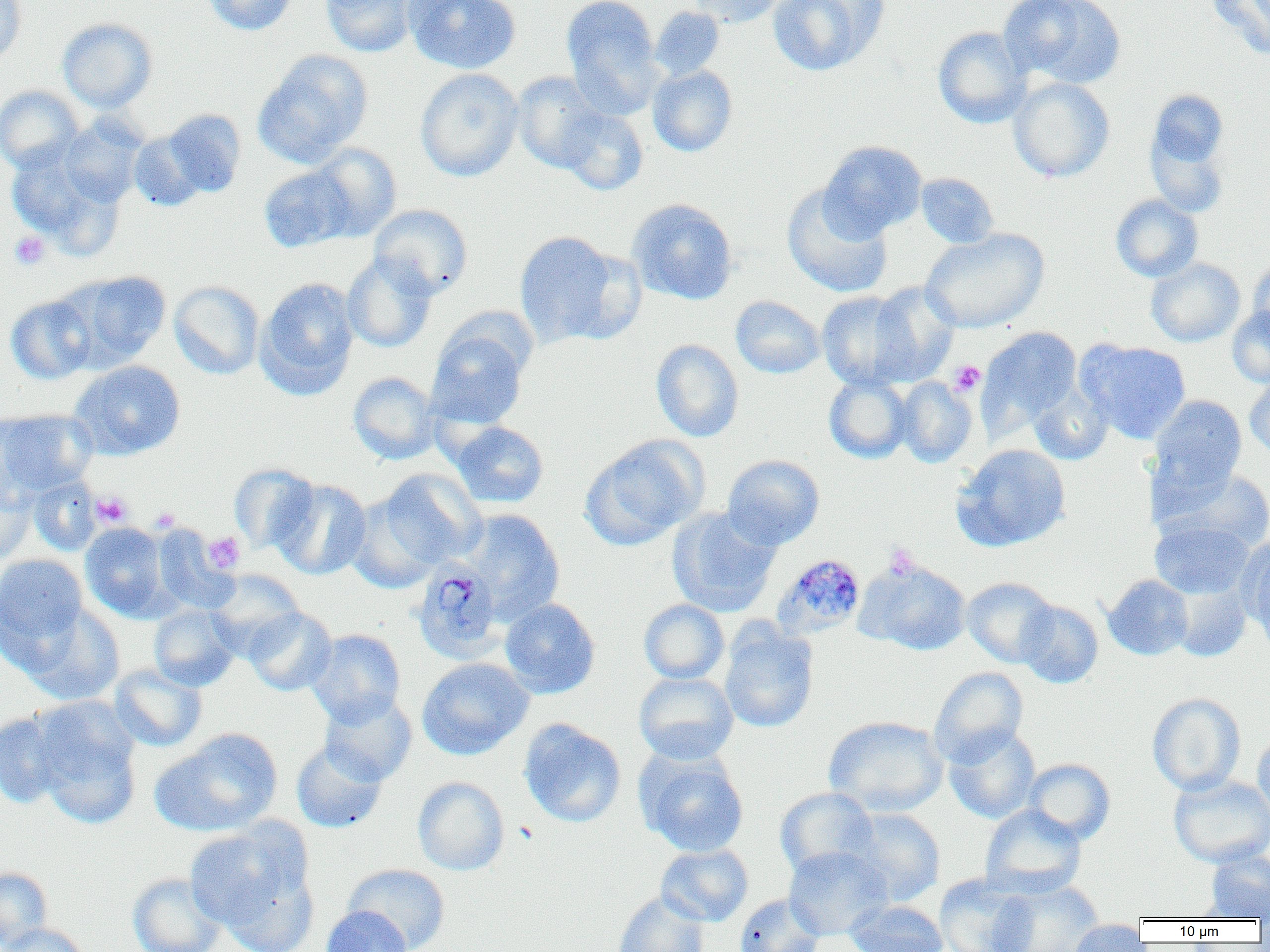 Approximate bounding boxes as (x1,y1)-(x2,y2) corner pairs in pixels. Uninfected red blood cell locations: (0,0)-(27,66), (202,0)-(298,36), (320,0)-(417,57), (404,0)-(521,74), (561,0)-(663,110), (689,0)-(789,27), (767,0)-(887,76), (998,0)-(1126,89), (1207,0)-(1270,58), (650,6)-(725,80), (57,18)-(158,112), (932,26)-(1032,128), (253,49)-(373,167), (648,65)-(738,156), (415,68)-(524,181), (511,72)-(606,172), (1008,77)-(1115,183), (0,85)-(85,173), (1143,88)-(1233,216), (556,105)-(648,196), (160,109)-(246,198), (56,118)-(146,207), (128,130)-(208,212), (819,141)-(927,239), (309,143)-(402,241), (6,146)-(124,254), (259,164)-(356,253), (915,173)-(999,248), (781,184)-(893,298), (1110,194)-(1203,282), (628,198)-(738,305), (369,204)-(473,299), (920,228)-(1049,332), (513,231)-(629,347), (342,252)-(438,353), (1146,258)-(1245,347), (1248,258)-(1270,344), (60,271)-(172,368), (257,276)-(360,399), (169,280)-(265,379), (866,282)-(960,385), (817,291)-(917,390), (5,294)-(97,385), (730,296)-(825,379), (1227,306)-(1270,387), (427,324)-(531,430), (978,327)-(1083,433), (651,339)-(744,442), (1078,339)-(1191,443), (70,360)-(186,460), (348,371)-(440,464), (824,374)-(914,463), (1244,374)-(1270,460), (894,376)-(978,467), (1028,383)-(1113,465), (1149,395)-(1247,493), (0,409)-(97,498), (451,421)-(549,508), (580,435)-(707,550), (953,443)-(1072,552), (722,454)-(825,549), (228,463)-(319,554), (1154,465)-(1270,556), (373,469)-(486,573), (28,475)-(102,555), (0,476)-(36,565), (271,478)-(372,579), (667,507)-(781,617), (459,509)-(566,621), (1149,520)-(1254,599), (80,521)-(171,621), (151,525)-(237,614), (1238,535)-(1270,641), (0,553)-(89,658), (855,557)-(972,656), (205,569)-(304,656), (1103,574)-(1194,660), (962,577)-(1058,668), (1169,579)-(1252,662), (500,598)-(600,698), (639,599)-(729,684), (1017,599)-(1104,688), (24,604)-(125,706), (149,604)-(240,691), (244,606)-(337,696), (718,620)-(819,733), (307,629)-(406,725), (416,657)-(534,760), (109,664)-(207,751), (929,666)-(1028,765), (633,672)-(739,764), (318,691)-(417,785), (1147,693)-(1246,795), (28,695)-(143,824), (0,711)-(71,808), (823,716)-(948,816), (519,719)-(626,828), (943,725)-(1041,824), (151,728)-(283,836), (1252,733)-(1270,824), (291,740)-(389,833), (636,748)-(749,857), (1023,758)-(1115,844), (1168,774)-(1270,867), (412,776)-(510,876), (775,787)-(879,878), (980,804)-(1086,898), (841,807)-(945,906), (186,821)-(316,945), (656,844)-(753,926), (783,845)-(892,940), (1204,848)-(1270,920), (341,863)-(451,952), (0,866)-(52,950), (127,872)-(227,952), (934,874)-(1037,952), (988,877)-(1105,952), (613,891)-(709,952), (733,893)-(824,952), (844,900)-(948,952), (320,905)-(413,952), (1064,920)-(1149,952), (2,922)-(89,951). Plasmodium malariae-infected red blood cell locations: (773,553)-(867,640), (416,557)-(507,661). Platelet locations: (9,231)-(51,270), (949,361)-(985,396), (91,492)-(132,526), (150,507)-(180,531), (203,532)-(244,573), (885,544)-(920,577). Slide-level diagnosis: Plasmodium malariae. Captured at 1000x magnification. Thin blood film. One field of a larger specimen. Image is 1270×952 pixels. Light microscopy.